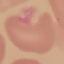

{
  "result": "no malaria parasites detected",
  "preparation": "thin blood smear",
  "image_type": "automatically extracted cell patch, resized to 64 × 64 pixels",
  "capture": "smartphone through the microscope eyepiece",
  "stain": "Giemsa"
}